Assess this cell for malaria.
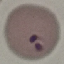
It is parasitized.

Summary:
  - Capture: smartphone through the microscope eyepiece
  - Preparation: thin blood film
  - Stain: Giemsa
  - Image type: cell patch, automatically extracted from a larger field of view and resized to 64 × 64 pixels